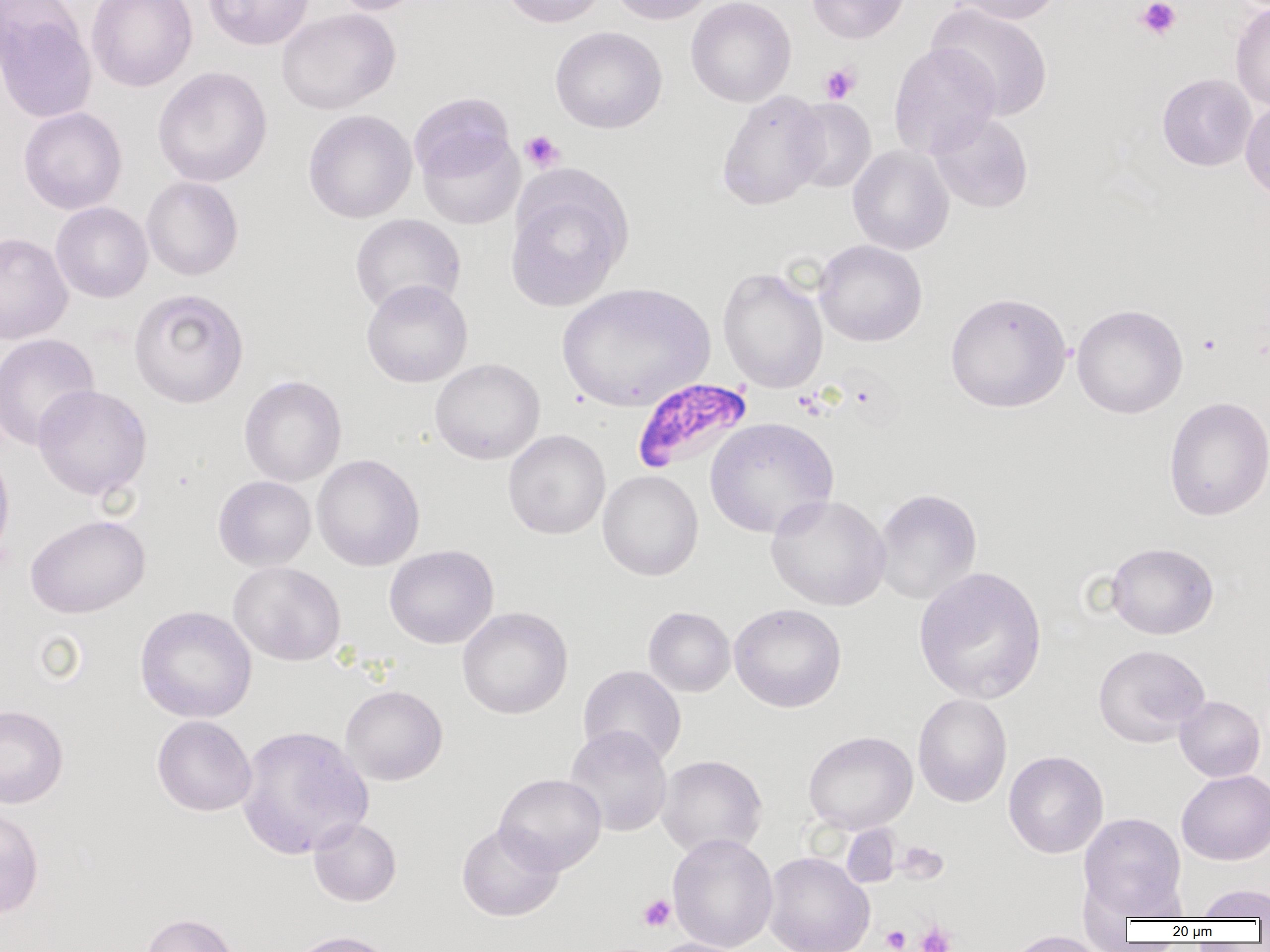
Summary:
  - Coordinate format: approximate bounding boxes as [x1, y1, x2, y2] in pixels
  - Uninfected red blood cell locations: [86, 0, 197, 92], [203, 0, 315, 51], [330, 0, 428, 15], [500, 0, 608, 27], [609, 0, 716, 25], [686, 0, 796, 107], [806, 0, 909, 44], [946, 0, 1065, 25], [1230, 2, 1270, 111], [926, 3, 1054, 121], [0, 6, 97, 124], [276, 8, 400, 115], [550, 26, 667, 133], [889, 42, 1001, 159], [152, 66, 273, 187], [1157, 73, 1257, 171], [716, 90, 828, 211], [409, 92, 515, 186], [787, 98, 877, 194], [1240, 99, 1270, 204], [18, 106, 127, 214], [303, 109, 417, 223], [928, 111, 1034, 213], [417, 130, 525, 230], [847, 145, 954, 255], [505, 171, 631, 311], [141, 176, 243, 281], [49, 191, 243, 289], [51, 202, 153, 303], [350, 214, 466, 315], [0, 232, 73, 345], [813, 240, 928, 346], [718, 267, 828, 394], [361, 279, 473, 388], [557, 282, 715, 412], [128, 287, 249, 407], [945, 291, 1072, 413], [1071, 304, 1188, 419], [0, 332, 99, 451], [430, 358, 545, 464], [239, 375, 346, 487], [32, 384, 152, 500], [1163, 396, 1269, 521], [705, 417, 839, 538], [503, 429, 611, 540], [0, 445, 15, 567], [312, 454, 424, 571], [597, 469, 703, 580], [213, 475, 316, 571], [873, 488, 982, 605], [765, 494, 891, 611], [25, 514, 150, 618], [1105, 541, 1219, 639], [384, 545, 499, 649], [228, 561, 346, 666], [913, 566, 1047, 705], [728, 603, 847, 713], [134, 605, 257, 723], [643, 606, 736, 697], [457, 607, 573, 719], [1093, 644, 1209, 747], [577, 665, 687, 768], [340, 685, 448, 786], [913, 694, 1012, 807], [1174, 695, 1266, 782], [0, 704, 68, 808], [152, 715, 257, 816], [236, 724, 374, 860], [563, 725, 673, 837], [803, 730, 918, 834], [1003, 750, 1108, 858], [656, 755, 767, 859], [1176, 769, 1270, 865], [494, 773, 607, 875], [0, 804, 44, 919], [1079, 812, 1187, 918], [308, 817, 401, 907], [456, 822, 564, 922], [841, 824, 900, 888], [667, 833, 778, 952], [763, 851, 874, 952], [1193, 883, 1270, 920], [139, 912, 242, 952], [283, 930, 400, 952], [1000, 931, 1112, 952], [644, 937, 756, 952]
  - Platelet locations: [1135, 0, 1182, 40], [819, 62, 861, 104], [520, 130, 565, 172], [1197, 333, 1221, 355], [638, 894, 676, 932], [914, 920, 957, 952], [881, 925, 910, 951]
  - Plasmodium falciparum-infected red blood cell locations: [632, 377, 754, 475]
  - Slide-level diagnosis: Plasmodium falciparum
  - Magnification: 1000x
  - Field of view: single
  - Preparation: thin blood film
  - Image size: 1270×952 pixels
  - Modality: light microscopy